Report the malaria status of this cell.
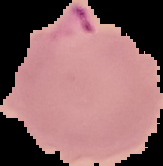
Parasitized.

preparation = thin blood film
image size = 163×166 pixels
image type = segmented cell region on a black background